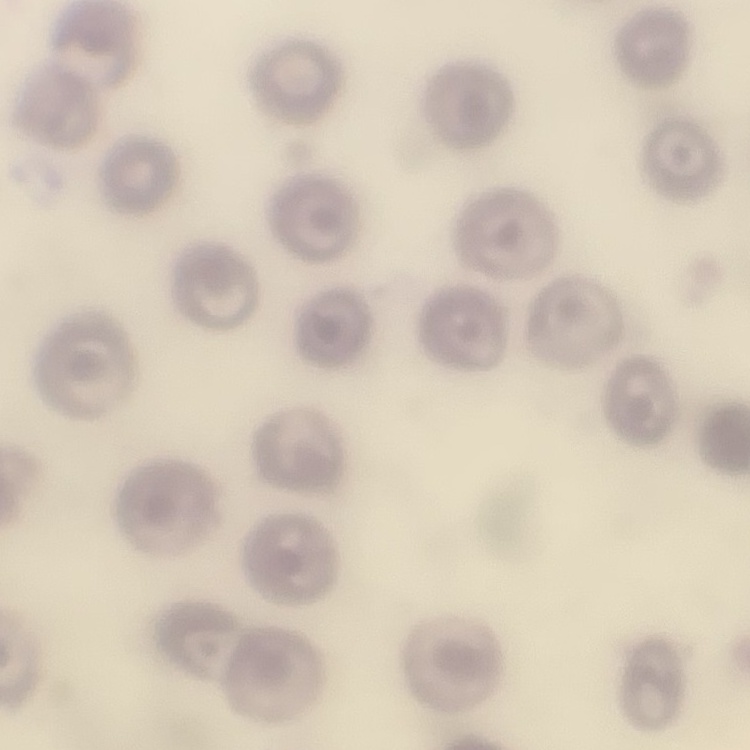

red blood cell morphology = no rouleaux formation
image type = one tile cut from a larger photomicrograph
preparation = thin peripheral smear
stain = Field's or Giemsa